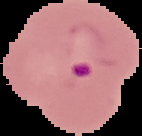

image size = 142×136 pixels
preparation = thin blood smear
image type = cell region segmented out of the field of view; surrounding area masked to black
result = Plasmodium parasites detected